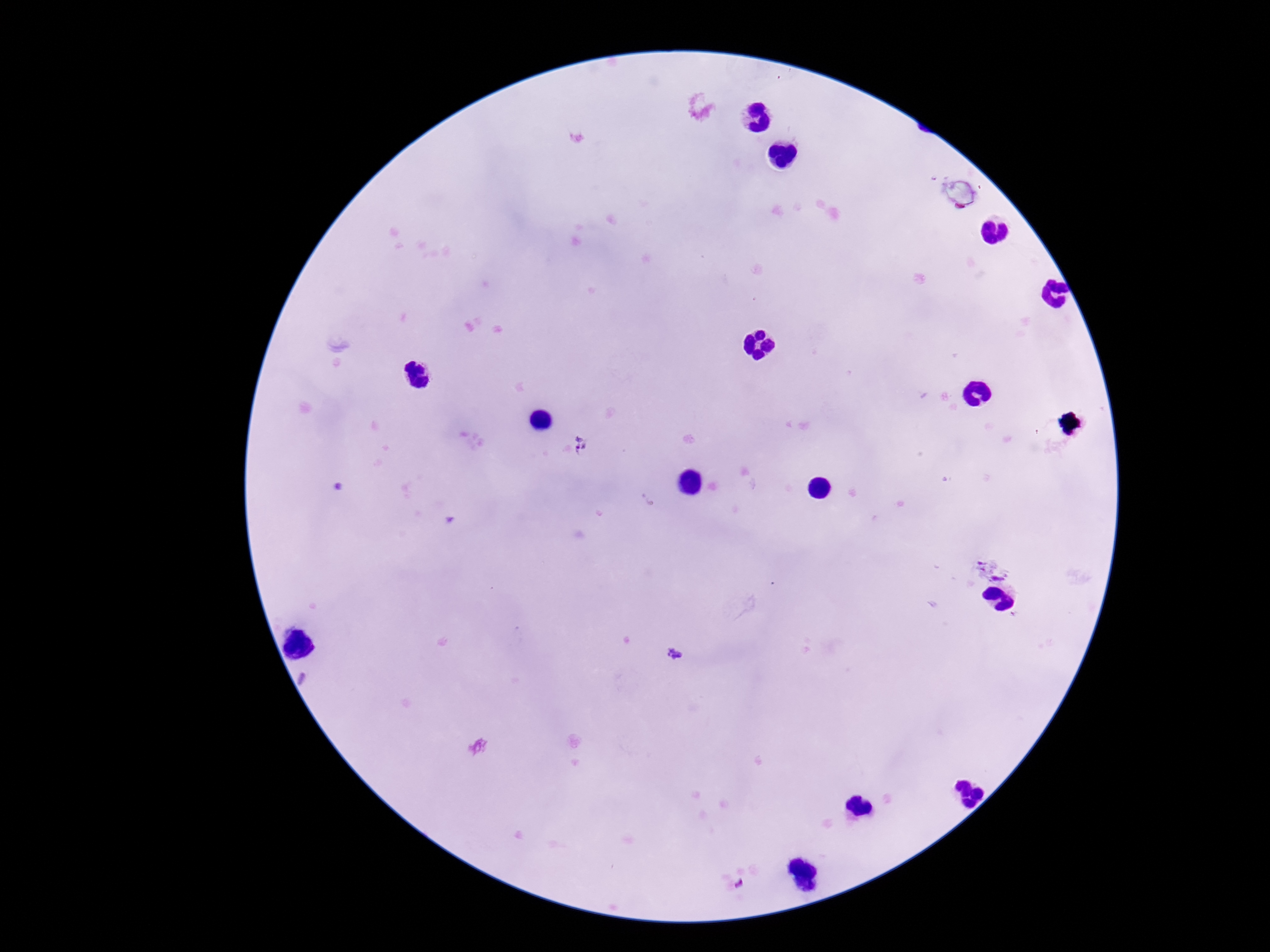

Approximate centers as [x, y] in pixels.
Summary:
  - Plasmodium parasite locations: [583, 446], [674, 655]
  - Preparation: thick blood smear
  - Stain: Giemsa
  - Capture: smartphone camera through the microscope eyepiece
  - Image size: 1270×952 pixels
  - Magnification: 100x
  - Field of view: single
  - Patient malaria status: positive